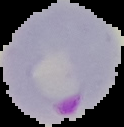 Segmented cell region on a black background. Malaria status: parasitized. Image is 124×127 pixels. From a thin blood film.